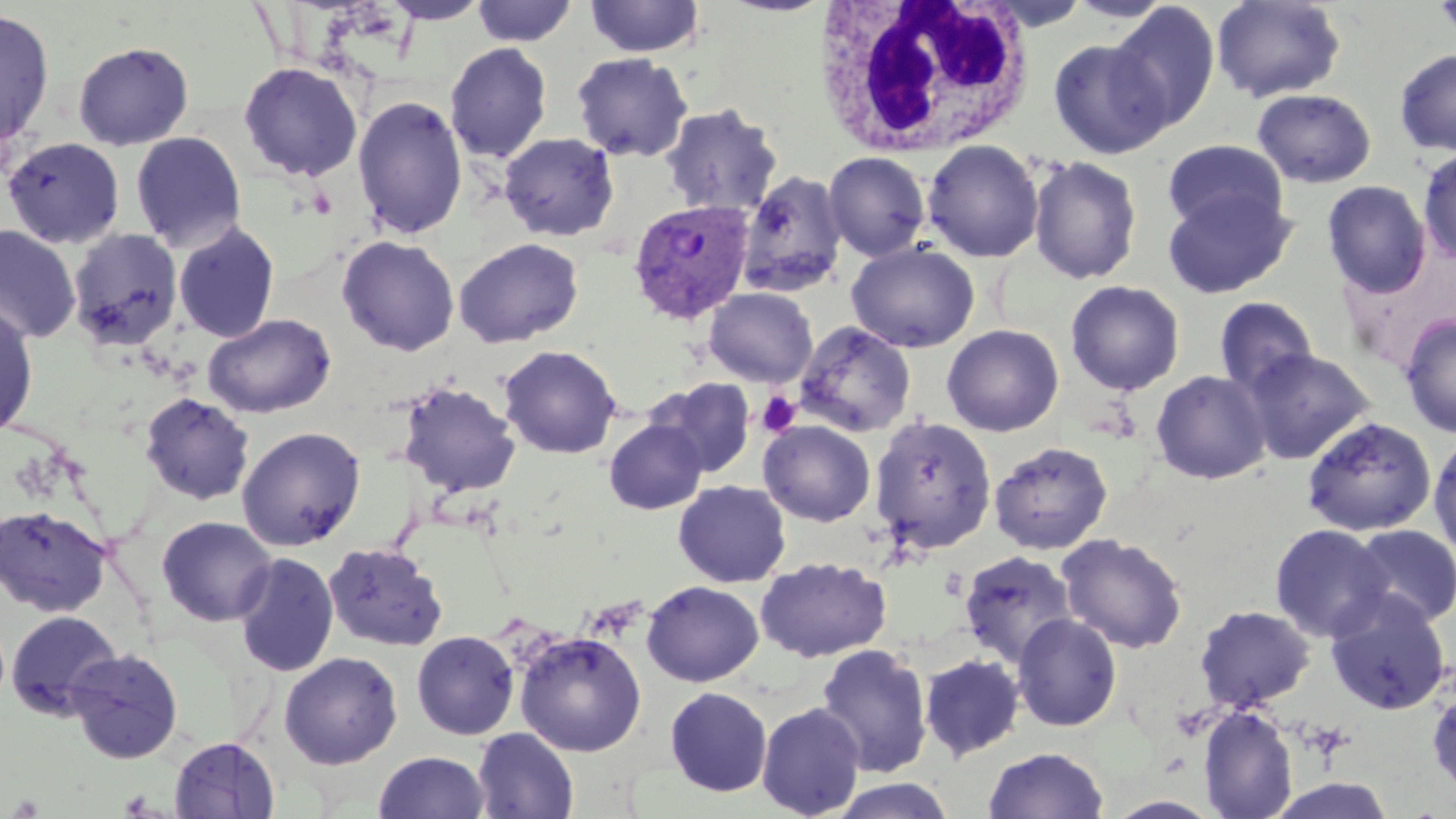
slide_level_diagnosis: Plasmodium vivax
white_blood_cell_locations: 'approximate bounding boxes as (x1,y1)-(x2,y2) corner pairs in pixels: (813,0)-(1037,157)'
stain: May-Grünwald-Giemsa
magnification: 1000x
plasmodium_vivax_infected_red_blood_cell_locations: 'approximate bounding boxes as (x1,y1)-(x2,y2) corner pairs in pixels: (627,198)-(755,324)'
field_of_view: one of a larger specimen
image_size: 1456×819 pixels
uninfected_red_blood_cell_locations: 'approximate bounding boxes as (x1,y1)-(x2,y2) corner pairs in pixels: (379,0)-(491,25), (584,0)-(705,58), (1065,0)-(1176,23), (1211,0)-(1347,103), (1433,0)-(1456,46), (471,1)-(578,46), (1107,2)-(1222,132), (0,9)-(56,152), (1048,39)-(1172,158), (72,41)-(194,150), (444,42)-(552,163), (1393,49)-(1456,156), (570,52)-(693,162), (238,62)-(363,181), (1252,88)-(1377,188), (352,95)-(468,240), (660,103)-(783,217), (130,131)-(247,252), (498,133)-(619,241), (1,136)-(126,250), (921,139)-(1044,262), (1161,140)-(1290,236), (1417,147)-(1456,266), (824,151)-(931,260), (1028,155)-(1143,285), (738,169)-(848,297), (1321,180)-(1432,297), (1162,186)-(1296,299), (172,222)-(280,343), (0,225)-(82,345), (67,229)-(183,354), (337,236)-(459,356), (453,238)-(584,348), (846,241)-(979,353), (1065,280)-(1185,396), (703,287)-(818,387), (1213,296)-(1318,397), (0,301)-(39,439), (203,313)-(336,419), (1399,314)-(1456,437), (793,321)-(917,437), (941,324)-(1064,437), (498,344)-(622,459), (1241,347)-(1376,465), (1151,370)-(1271,485), (650,378)-(756,478), (399,380)-(521,498), (138,393)-(255,507), (870,414)-(997,555), (1301,416)-(1437,536), (604,419)-(708,515), (758,420)-(876,526), (237,426)-(366,551), (1429,430)-(1456,563), (988,440)-(1113,554), (673,480)-(791,587), (0,504)-(112,617), (157,515)-(277,626), (1269,524)-(1392,642), (1348,524)-(1455,629), (1056,533)-(1189,654), (323,541)-(448,652), (958,550)-(1078,668), (233,552)-(339,677), (755,556)-(891,662), (642,580)-(764,687), (1324,588)-(1452,715), (1194,604)-(1316,712), (5,609)-(122,721), (1012,614)-(1123,732), (513,630)-(648,756), (411,631)-(520,740), (815,644)-(933,778), (65,647)-(184,763), (279,652)-(402,769), (918,653)-(1026,761), (1427,684)-(1456,799), (665,686)-(772,796), (756,702)-(865,818), (1199,704)-(1298,819), (472,728)-(578,818), (169,736)-(280,818), (983,747)-(1109,819), (374,751)-(490,818), (1264,776)-(1397,818), (829,778)-(956,819), (1104,795)-(1223,818)'
preparation: thin blood film
platelet_locations: 'approximate bounding boxes as (x1,y1)-(x2,y2) corner pairs in pixels: (757,391)-(801,437)'
modality: light microscopy